Locate every uninfected red blood cell.
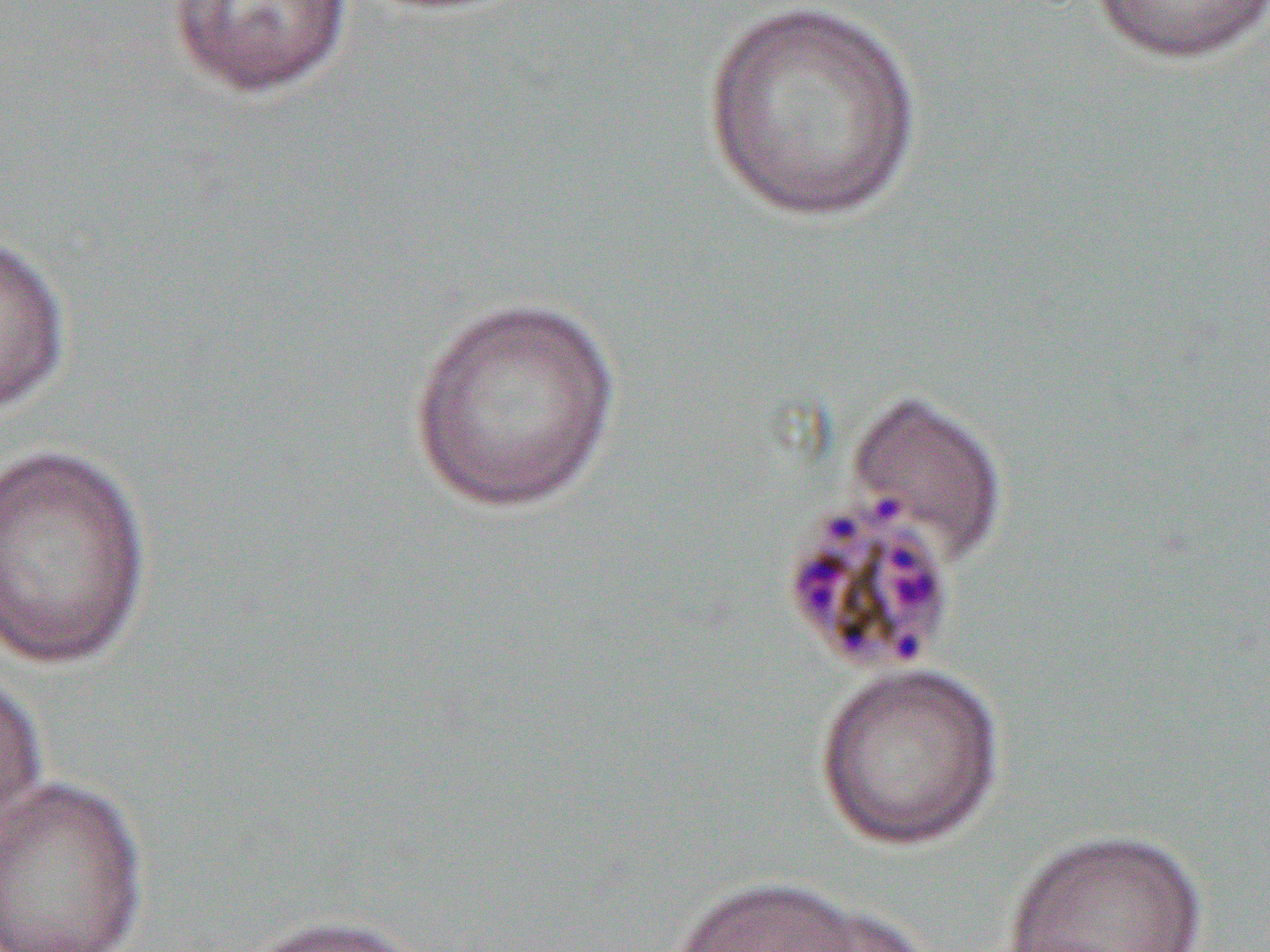
Approximate bounding boxes as [x1, y1, x2, y2] in pixels.
Uninfected red blood cells: [702, 0, 925, 224], [1088, 0, 1270, 65], [166, 1, 355, 101], [0, 232, 73, 417], [404, 295, 626, 514], [844, 387, 1010, 567], [1, 441, 154, 671], [812, 660, 1007, 851], [0, 668, 48, 846], [0, 775, 150, 952], [999, 827, 1211, 951], [656, 872, 923, 952], [240, 913, 432, 952].

Slide-level diagnosis: Plasmodium malariae. Light microscopy. Captured at 1000x magnification. Thin blood smear. One field of a larger specimen. Image is 1270×952 pixels.